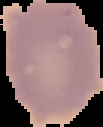
{
  "image_size": "103×127 pixels",
  "image_type": "cell region segmented out of the field of view; surrounding area masked to black",
  "malaria_status": "uninfected",
  "preparation": "thin blood smear"
}